Give the extent of all uninfected red blood cells.
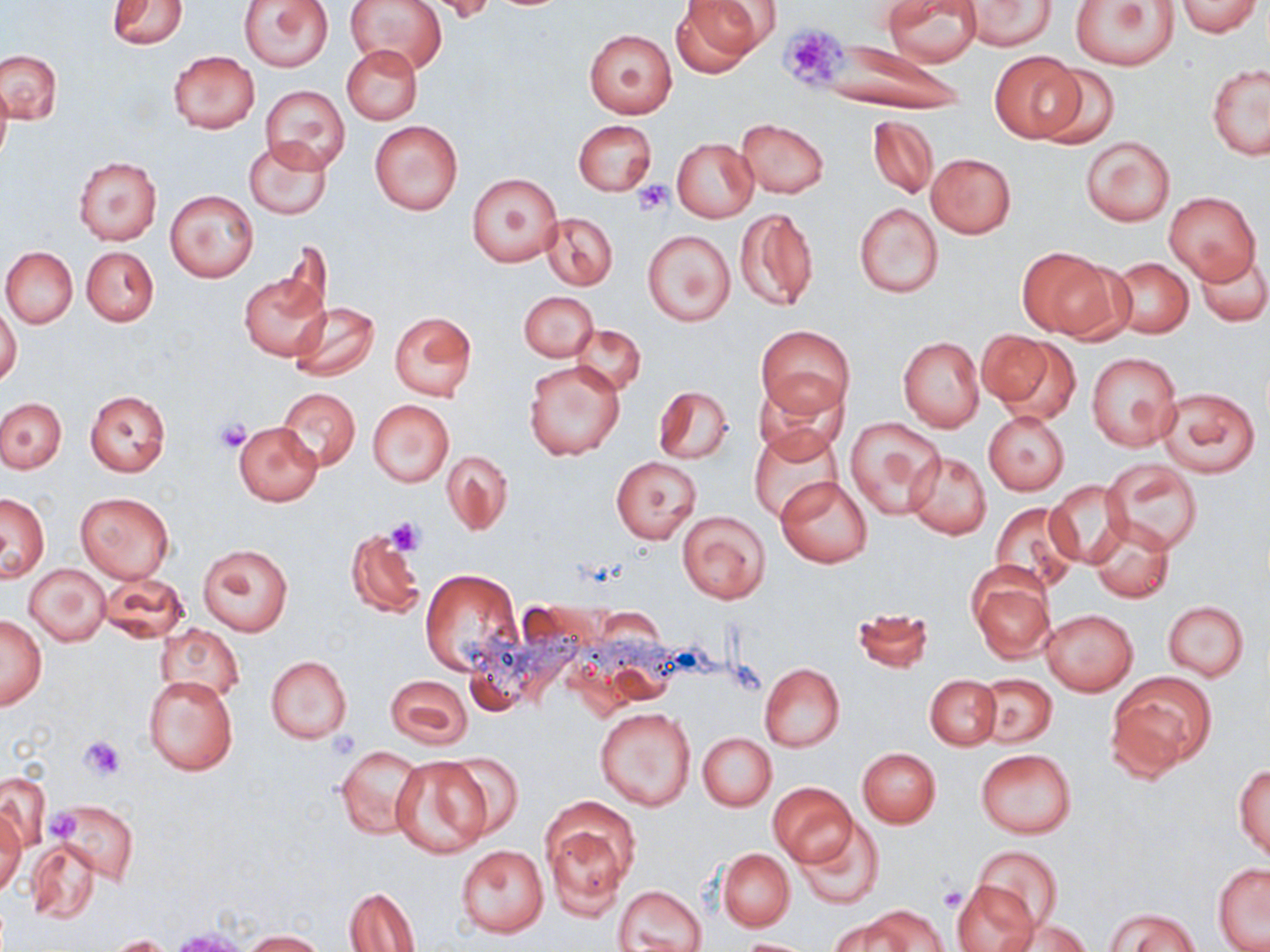

Approximate bounding boxes as named x1/y1/x2/y2 corners in pixels.
Uninfected red blood cells: (x1=238, y1=0, x2=333, y2=72), (x1=347, y1=0, x2=447, y2=74), (x1=423, y1=0, x2=502, y2=24), (x1=670, y1=0, x2=768, y2=76), (x1=882, y1=0, x2=981, y2=66), (x1=1069, y1=0, x2=1179, y2=71), (x1=106, y1=1, x2=188, y2=48), (x1=961, y1=1, x2=1056, y2=51), (x1=1175, y1=1, x2=1263, y2=36), (x1=584, y1=29, x2=677, y2=118), (x1=826, y1=37, x2=969, y2=117), (x1=342, y1=45, x2=422, y2=125), (x1=0, y1=49, x2=62, y2=123), (x1=168, y1=51, x2=260, y2=134), (x1=989, y1=51, x2=1086, y2=142), (x1=1207, y1=63, x2=1270, y2=162), (x1=1035, y1=64, x2=1123, y2=149), (x1=0, y1=75, x2=11, y2=169), (x1=261, y1=85, x2=350, y2=173), (x1=867, y1=115, x2=938, y2=198), (x1=736, y1=118, x2=828, y2=198), (x1=369, y1=120, x2=463, y2=216), (x1=573, y1=120, x2=656, y2=195), (x1=1080, y1=134, x2=1174, y2=227), (x1=672, y1=138, x2=758, y2=223), (x1=245, y1=139, x2=332, y2=220), (x1=927, y1=152, x2=1016, y2=238), (x1=72, y1=155, x2=162, y2=245), (x1=467, y1=174, x2=562, y2=267), (x1=164, y1=189, x2=260, y2=282), (x1=1163, y1=190, x2=1262, y2=287), (x1=854, y1=203, x2=943, y2=297), (x1=734, y1=207, x2=818, y2=312), (x1=541, y1=214, x2=617, y2=290), (x1=642, y1=230, x2=734, y2=326), (x1=1, y1=246, x2=77, y2=327), (x1=82, y1=247, x2=159, y2=326), (x1=1017, y1=247, x2=1125, y2=340), (x1=1194, y1=251, x2=1269, y2=326), (x1=1109, y1=257, x2=1194, y2=339), (x1=240, y1=271, x2=328, y2=360), (x1=519, y1=291, x2=598, y2=361), (x1=289, y1=302, x2=380, y2=381), (x1=0, y1=305, x2=22, y2=388), (x1=388, y1=311, x2=477, y2=401), (x1=570, y1=324, x2=645, y2=397), (x1=757, y1=324, x2=854, y2=418), (x1=981, y1=330, x2=1078, y2=423), (x1=899, y1=336, x2=983, y2=432), (x1=1086, y1=352, x2=1181, y2=451), (x1=524, y1=361, x2=625, y2=461), (x1=753, y1=375, x2=847, y2=460), (x1=654, y1=385, x2=734, y2=465), (x1=1156, y1=386, x2=1261, y2=478), (x1=278, y1=388, x2=359, y2=471), (x1=85, y1=390, x2=169, y2=476), (x1=0, y1=398, x2=66, y2=473), (x1=367, y1=399, x2=454, y2=487), (x1=983, y1=411, x2=1070, y2=495), (x1=844, y1=416, x2=945, y2=518), (x1=233, y1=421, x2=324, y2=506), (x1=750, y1=428, x2=841, y2=522), (x1=443, y1=449, x2=512, y2=537), (x1=905, y1=451, x2=991, y2=539), (x1=611, y1=456, x2=701, y2=544), (x1=1104, y1=461, x2=1203, y2=551), (x1=776, y1=476, x2=872, y2=568), (x1=1045, y1=479, x2=1132, y2=567), (x1=1, y1=491, x2=50, y2=582), (x1=74, y1=491, x2=175, y2=582), (x1=989, y1=503, x2=1078, y2=593), (x1=675, y1=510, x2=770, y2=605), (x1=1087, y1=516, x2=1175, y2=603), (x1=345, y1=528, x2=425, y2=618), (x1=196, y1=544, x2=292, y2=636), (x1=24, y1=563, x2=111, y2=646), (x1=967, y1=566, x2=1056, y2=664), (x1=419, y1=569, x2=521, y2=675), (x1=97, y1=572, x2=188, y2=643), (x1=1163, y1=601, x2=1248, y2=681), (x1=851, y1=606, x2=934, y2=675), (x1=1041, y1=609, x2=1138, y2=696), (x1=0, y1=613, x2=47, y2=711), (x1=156, y1=626, x2=244, y2=705), (x1=264, y1=655, x2=353, y2=743), (x1=758, y1=662, x2=844, y2=752), (x1=1110, y1=673, x2=1214, y2=774), (x1=386, y1=674, x2=472, y2=749), (x1=925, y1=674, x2=1001, y2=751), (x1=977, y1=674, x2=1057, y2=748), (x1=143, y1=676, x2=239, y2=776), (x1=595, y1=707, x2=694, y2=811), (x1=697, y1=732, x2=777, y2=810), (x1=336, y1=746, x2=424, y2=839), (x1=857, y1=748, x2=941, y2=828), (x1=976, y1=749, x2=1077, y2=838), (x1=436, y1=752, x2=526, y2=840), (x1=389, y1=759, x2=492, y2=858), (x1=1234, y1=764, x2=1270, y2=861), (x1=0, y1=773, x2=50, y2=852), (x1=768, y1=783, x2=857, y2=867), (x1=541, y1=799, x2=637, y2=918), (x1=52, y1=801, x2=138, y2=883), (x1=0, y1=807, x2=26, y2=898), (x1=796, y1=818, x2=886, y2=912), (x1=24, y1=839, x2=103, y2=926), (x1=455, y1=844, x2=550, y2=938), (x1=973, y1=846, x2=1064, y2=930), (x1=718, y1=848, x2=794, y2=932), (x1=1213, y1=864, x2=1270, y2=951), (x1=952, y1=879, x2=1040, y2=952), (x1=614, y1=885, x2=708, y2=952), (x1=346, y1=887, x2=421, y2=951), (x1=860, y1=906, x2=947, y2=952), (x1=1107, y1=908, x2=1200, y2=952), (x1=998, y1=916, x2=1093, y2=951), (x1=827, y1=918, x2=910, y2=952), (x1=241, y1=930, x2=328, y2=951), (x1=104, y1=934, x2=177, y2=952), (x1=736, y1=938, x2=817, y2=951).

slide-level diagnosis = negative for blood parasites
platelet locations = approximate bounding boxes as named x1/y1/x2/y2 corners in pixels: (x1=778, y1=23, x2=850, y2=90), (x1=632, y1=180, x2=672, y2=216), (x1=214, y1=418, x2=253, y2=453), (x1=385, y1=517, x2=427, y2=556), (x1=80, y1=735, x2=125, y2=779), (x1=49, y1=807, x2=81, y2=841), (x1=939, y1=884, x2=966, y2=912)
magnification = 1000x
modality = optical microscopy
field of view = one of a larger specimen
stain = May-Grünwald-Giemsa
preparation = thin blood film
image size = 1270×952 pixels